Give the location of every parasitized red blood cell.
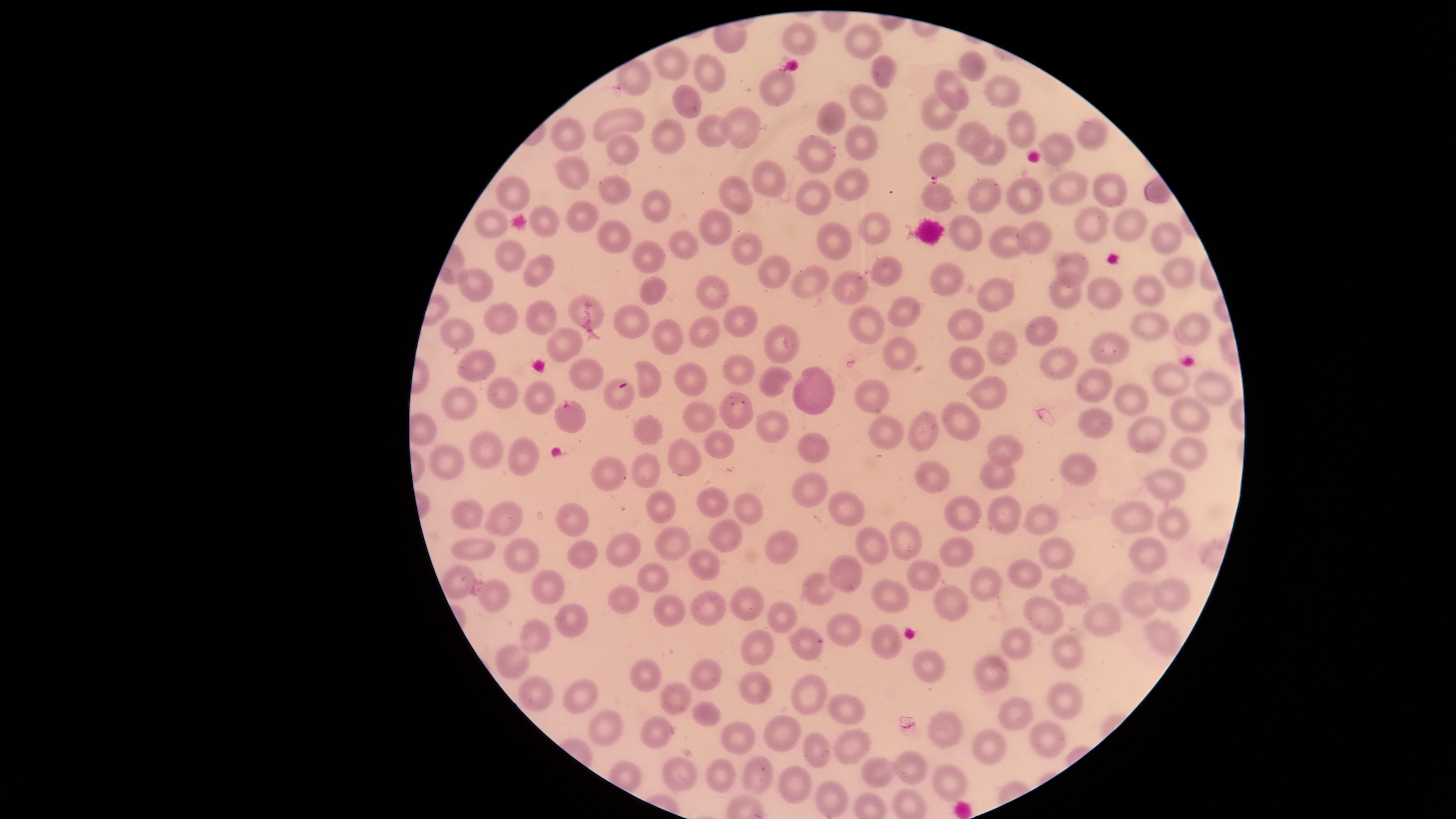

Approximate marker points as (x, y) in pixels.
Parasitized red blood cells: (568, 409).

Approximate marker points as (x, y) in pixels. Uninfected red blood cells: (797, 37), (866, 45), (676, 65), (972, 65), (879, 72), (710, 73), (636, 78), (774, 82), (952, 90), (1001, 95), (684, 103), (867, 105), (934, 112), (830, 116), (619, 121), (738, 125), (971, 130), (1025, 132), (712, 135), (1096, 135), (566, 136), (675, 139), (617, 147), (860, 148), (1060, 151), (997, 154), (819, 157), (937, 159), (568, 173), (770, 177), (1061, 183), (611, 185), (853, 186), (1108, 191), (983, 194), (518, 196), (1020, 197), (737, 198), (938, 199), (818, 201), (652, 204), (581, 217), (1093, 222), (493, 223), (541, 224), (1130, 225), (874, 226), (714, 228), (1158, 230), (1036, 234), (973, 237), (612, 238), (835, 241), (675, 242), (1000, 246), (745, 252), (505, 255), (653, 259), (1078, 267), (544, 271), (884, 271), (1175, 274), (773, 275), (949, 278), (476, 281), (814, 283), (852, 287), (655, 292), (1107, 292), (1143, 292), (712, 295), (995, 295), (1069, 299), (577, 309), (899, 309), (497, 313), (537, 313), (634, 316), (734, 323), (973, 324), (866, 325), (1155, 329), (1190, 329), (705, 333), (459, 335), (1034, 335), (663, 338), (568, 342), (782, 343), (1107, 349), (1008, 350), (896, 354), (1056, 359), (965, 367), (478, 368), (738, 373), (583, 374), (653, 377), (693, 378), (1173, 381), (770, 383), (1209, 385), (1096, 386), (811, 388), (505, 393), (620, 395), (872, 398), (998, 398), (536, 399), (1124, 400), (464, 401), (744, 411), (1186, 417), (1103, 419), (703, 420), (962, 422), (646, 428), (770, 428), (921, 430), (1147, 430), (888, 432), (715, 441), (806, 441), (999, 446), (494, 448), (527, 453), (1185, 453), (682, 458), (443, 462), (1084, 464), (931, 465), (647, 467), (600, 470), (993, 471), (1167, 484), (801, 488), (716, 507), (748, 507), (840, 507), (665, 508), (993, 511), (958, 517), (473, 520), (1133, 521), (1172, 521), (506, 522), (573, 523), (1044, 525), (722, 540), (1146, 543), (903, 545), (577, 546), (775, 546), (666, 549), (869, 549), (473, 550), (1052, 550), (630, 552), (519, 556), (956, 557), (703, 564), (850, 570), (1020, 571), (648, 575), (926, 579), (978, 581), (459, 582), (542, 586), (1076, 587), (822, 590), (1167, 594), (493, 597), (1133, 598), (621, 600), (740, 602), (949, 603), (883, 604), (779, 609), (706, 610), (675, 614), (1045, 615), (1099, 616), (568, 617), (845, 629), (1159, 631), (532, 635), (883, 638), (803, 639), (1015, 641), (755, 646), (1069, 650), (510, 659), (919, 662), (651, 674), (709, 674), (982, 676), (755, 690), (533, 695), (577, 696), (807, 696), (1059, 697), (670, 699), (1017, 706), (703, 713), (844, 715), (949, 725), (600, 727), (665, 727), (734, 732), (779, 733), (1048, 737), (846, 744), (814, 746), (989, 750), (680, 767), (720, 767), (756, 767), (918, 768), (872, 772), (948, 777), (796, 782), (831, 797). Photographed with a smartphone camera through the microscope eyepiece. Species: Plasmodium falciparum. Giemsa stain. The visible region is circular. One field of view of the specimen. Thin blood smear. Image is 1456×819 pixels.